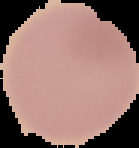

image type = cell region segmented out of the field of view; surrounding area masked to black
malaria status = uninfected
image size = 139×148 pixels
preparation = thin blood film